Outline each Plasmodium malariae-infected red blood cell.
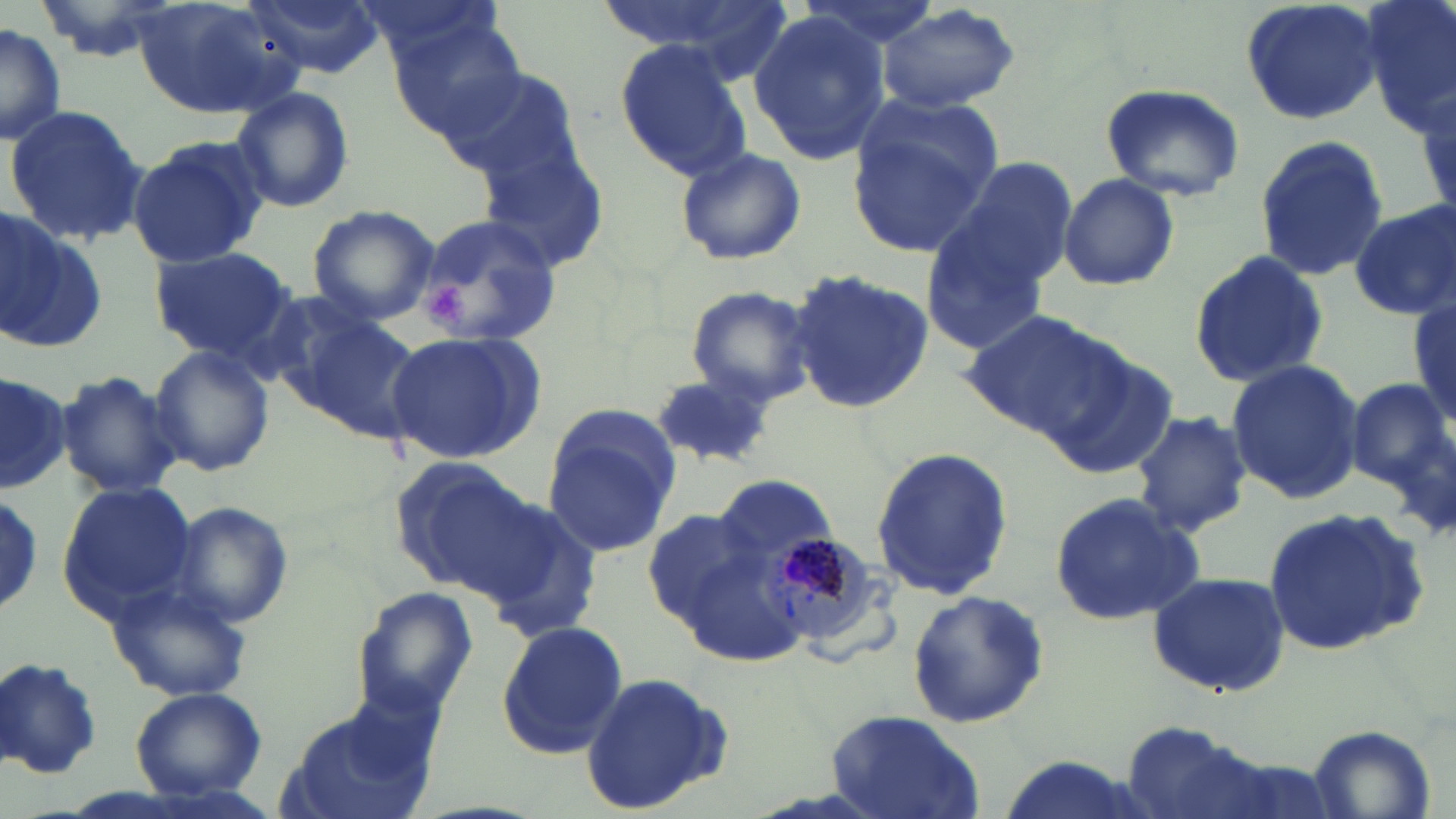

Approximate bounding boxes as (x1,y1)-(x2,y2) corner pairs in pixels.
Plasmodium malariae-infected red blood cells: (762,534)-(882,646).

Uninfected red blood cell locations: (130,0)-(297,118), (246,0)-(385,79), (594,0)-(785,79), (796,0)-(944,54), (1241,0)-(1384,126), (1362,0)-(1455,139), (351,1)-(503,72), (875,5)-(1021,114), (749,9)-(887,167), (0,23)-(65,147), (394,29)-(533,147), (613,36)-(754,183), (446,70)-(583,184), (1098,82)-(1246,202), (228,87)-(356,214), (848,100)-(1002,254), (4,105)-(150,246), (1253,135)-(1388,283), (126,136)-(268,269), (477,145)-(612,274), (673,146)-(806,267), (944,155)-(1079,287), (1059,172)-(1181,291), (1349,202)-(1456,321), (306,204)-(441,326), (1,213)-(109,354), (917,214)-(1057,358), (412,216)-(559,344), (147,245)-(300,364), (1188,250)-(1328,391), (788,270)-(937,414), (685,285)-(816,407), (1409,291)-(1455,429), (955,307)-(1125,443), (299,311)-(424,444), (384,332)-(544,467), (149,344)-(274,478), (1047,351)-(1179,481), (1225,358)-(1365,505), (56,369)-(182,501), (0,370)-(68,495), (1349,372)-(1456,513), (649,374)-(778,472), (1129,409)-(1252,537), (542,424)-(678,557), (870,447)-(1013,605), (389,458)-(544,596), (714,475)-(836,568), (55,482)-(197,618), (1049,491)-(1207,626), (0,494)-(44,614), (167,501)-(295,628), (473,504)-(603,642), (642,507)-(774,640), (1259,509)-(1426,657), (1146,570)-(1291,699), (105,577)-(254,702), (352,587)-(479,721), (904,590)-(1051,727), (494,620)-(627,760), (0,657)-(103,780), (577,672)-(734,815), (130,688)-(268,803), (276,695)-(447,819), (823,711)-(985,819), (1121,720)-(1269,819), (1307,725)-(1437,819). Platelet locations: (427,279)-(464,324). Slide-level diagnosis: Plasmodium malariae. 1000x magnification. Single field of view. Thin blood film. May-Grünwald-Giemsa-stained preparation. Optical microscopy. Image is 1456×819 pixels.